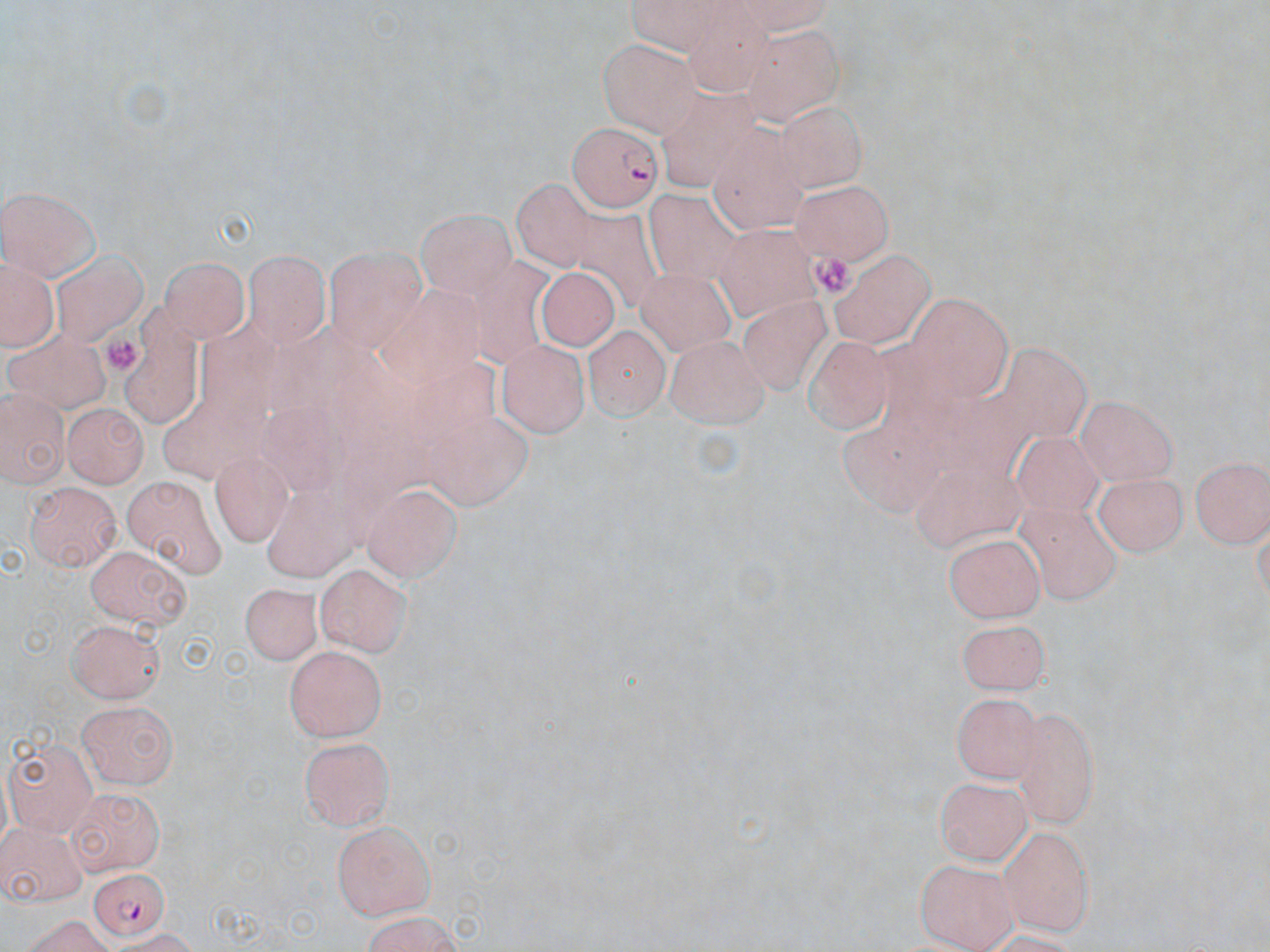

slide-level diagnosis = Plasmodium falciparum
image size = 1270×952 pixels
platelet locations = approximate bounding boxes as named x1/y1/x2/y2 corners in pixels: (x1=810, y1=252, x2=858, y2=302), (x1=103, y1=335, x2=140, y2=378)
modality = light microscopy
preparation = thin blood film
stain = May-Grünwald-Giemsa
Plasmodium falciparum-infected red blood cell locations = approximate bounding boxes as named x1/y1/x2/y2 corners in pixels: (x1=566, y1=118, x2=665, y2=211), (x1=87, y1=863, x2=165, y2=940)
magnification = 1000x
uninfected red blood cell locations = approximate bounding boxes as named x1/y1/x2/y2 corners in pixels: (x1=743, y1=29, x2=843, y2=125), (x1=595, y1=42, x2=705, y2=138), (x1=710, y1=110, x2=809, y2=230), (x1=510, y1=178, x2=598, y2=274), (x1=789, y1=182, x2=895, y2=264), (x1=1, y1=183, x2=101, y2=274), (x1=642, y1=187, x2=743, y2=282), (x1=569, y1=205, x2=665, y2=309), (x1=415, y1=210, x2=516, y2=296), (x1=324, y1=242, x2=430, y2=354), (x1=831, y1=246, x2=931, y2=344), (x1=243, y1=248, x2=331, y2=349), (x1=52, y1=251, x2=149, y2=345), (x1=162, y1=257, x2=248, y2=341), (x1=5, y1=260, x2=56, y2=349), (x1=541, y1=269, x2=621, y2=350), (x1=635, y1=270, x2=733, y2=357), (x1=737, y1=295, x2=838, y2=397), (x1=128, y1=302, x2=204, y2=428), (x1=589, y1=322, x2=671, y2=418), (x1=2, y1=325, x2=110, y2=419), (x1=801, y1=334, x2=895, y2=435), (x1=664, y1=337, x2=772, y2=435), (x1=498, y1=339, x2=589, y2=438), (x1=1, y1=387, x2=68, y2=487), (x1=1078, y1=393, x2=1179, y2=480), (x1=61, y1=404, x2=143, y2=488), (x1=1010, y1=425, x2=1103, y2=523), (x1=207, y1=449, x2=289, y2=538), (x1=1188, y1=453, x2=1267, y2=549), (x1=1091, y1=470, x2=1188, y2=556), (x1=123, y1=473, x2=227, y2=585), (x1=361, y1=476, x2=464, y2=581), (x1=23, y1=481, x2=123, y2=571), (x1=1008, y1=502, x2=1127, y2=609), (x1=946, y1=531, x2=1047, y2=621), (x1=86, y1=545, x2=192, y2=629), (x1=315, y1=564, x2=413, y2=657), (x1=238, y1=579, x2=321, y2=663), (x1=957, y1=613, x2=1052, y2=693), (x1=66, y1=615, x2=166, y2=700), (x1=286, y1=644, x2=388, y2=742), (x1=952, y1=690, x2=1043, y2=786), (x1=77, y1=699, x2=179, y2=787), (x1=1009, y1=701, x2=1106, y2=829), (x1=296, y1=735, x2=396, y2=831), (x1=5, y1=736, x2=93, y2=833), (x1=936, y1=774, x2=1034, y2=862), (x1=57, y1=787, x2=163, y2=873), (x1=0, y1=821, x2=85, y2=906), (x1=331, y1=821, x2=437, y2=920), (x1=999, y1=824, x2=1098, y2=936), (x1=914, y1=856, x2=1022, y2=950), (x1=352, y1=914, x2=468, y2=952), (x1=16, y1=917, x2=121, y2=951)
field of view = single